Evaluate for parasitized red blood cells.
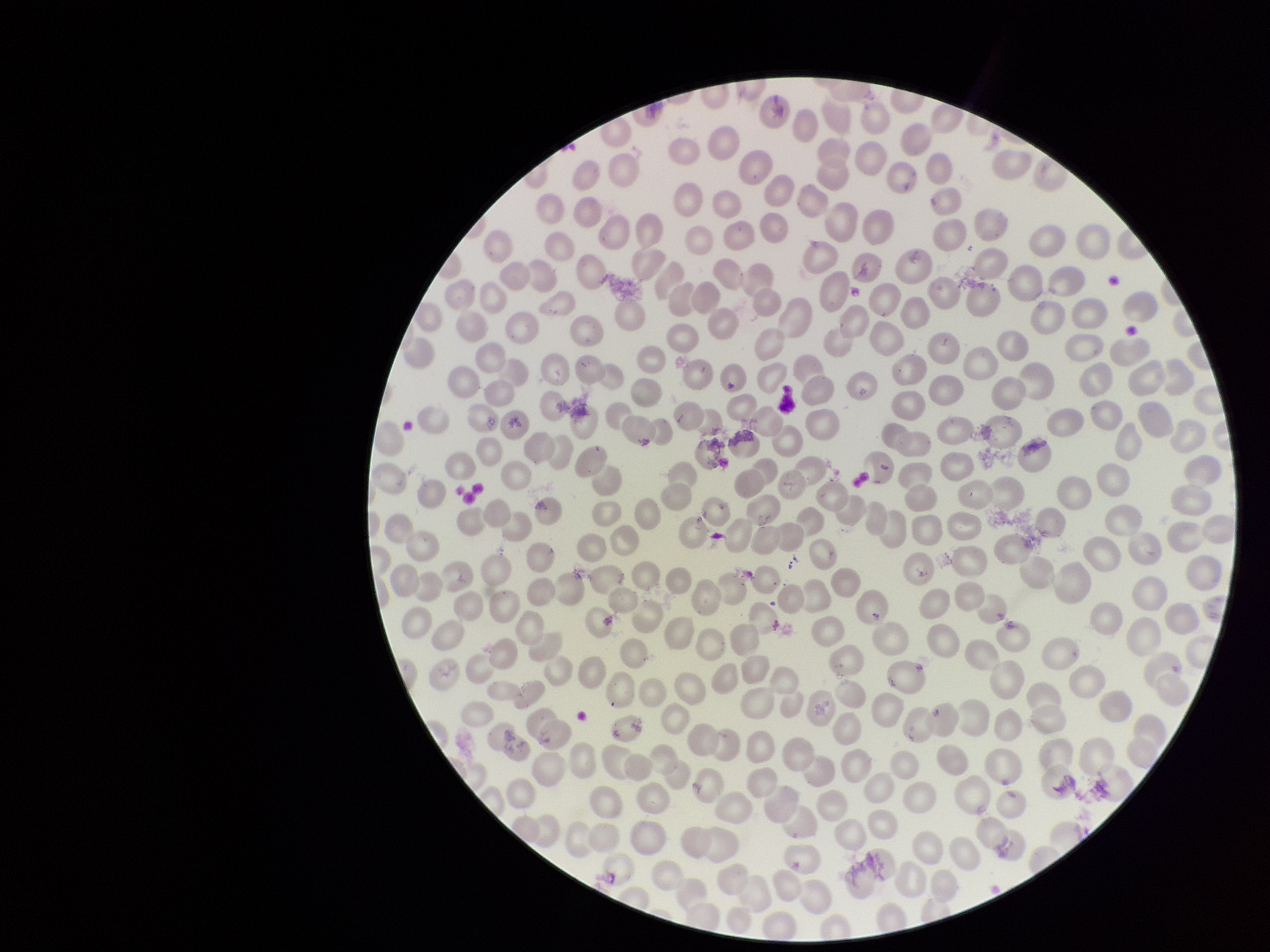

None seen.

Preparation: thin blood smear. Red blood cell count: 276. Stained with Giemsa. One field from this slide. Parasitized red blood cell count: 0. Patient malaria status: negative. Image is 1270×952 pixels. Smartphone photograph taken through the eyepiece of a microscope.